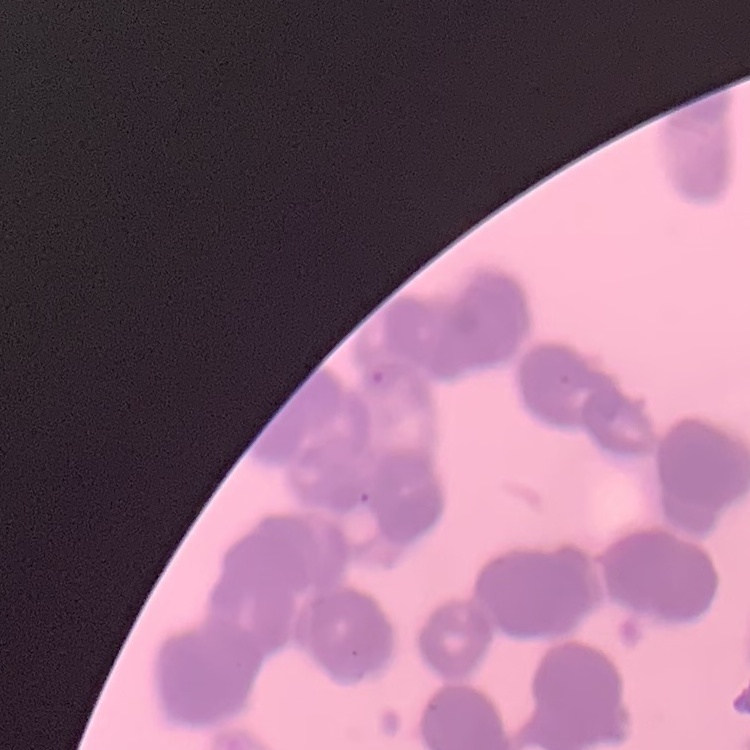 The erythrocytes exhibit rouleaux formation. Square crop of a larger photomicrograph. Thin blood film. Stained with either Field's or Giemsa.